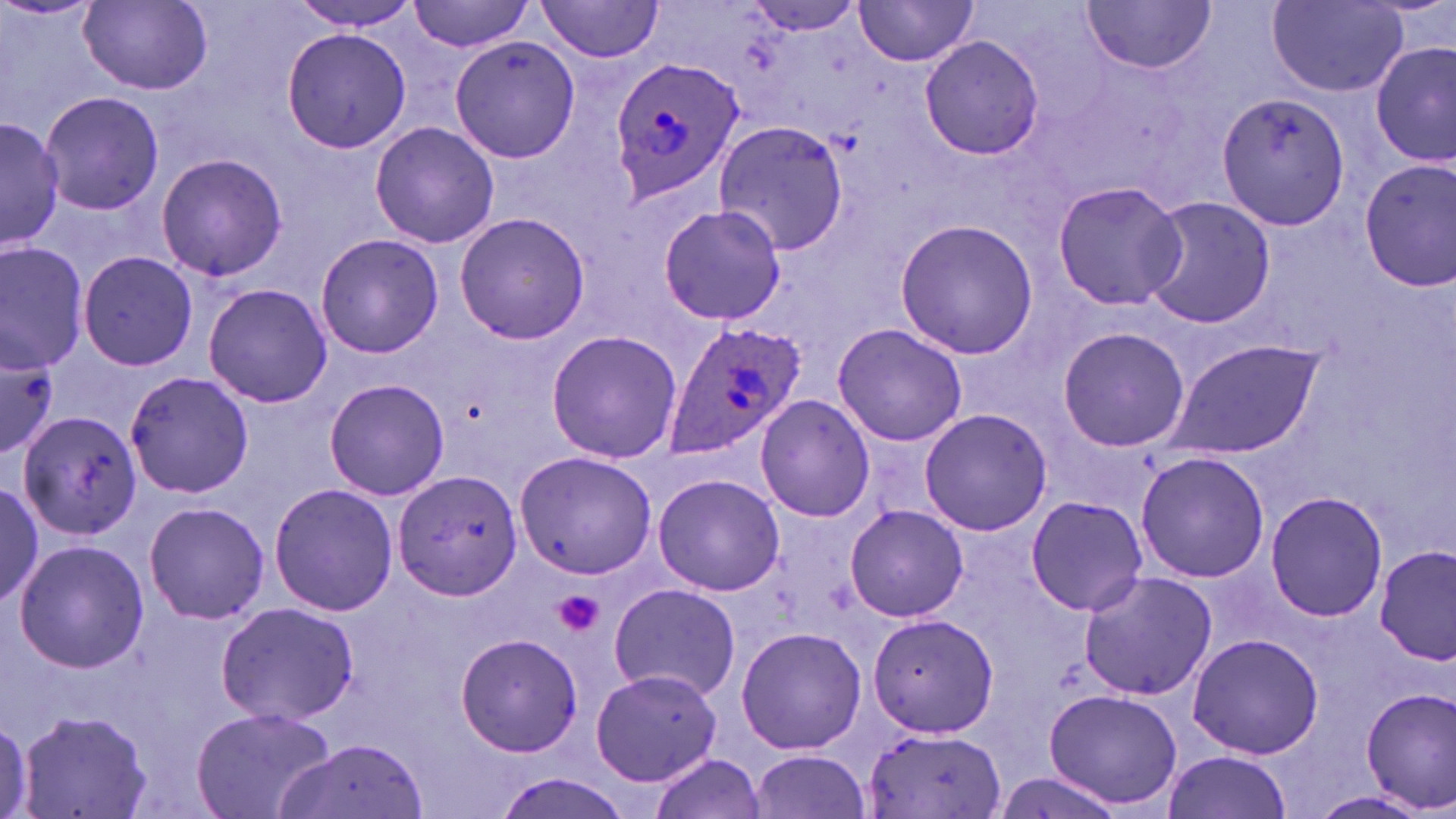
slide-level diagnosis = Plasmodium ovale
stain = May-Grünwald-Giemsa
image size = 1456×819 pixels
platelet locations = approximate bounding boxes as [x1, y1, x2, y2] in pixels: [553, 590, 604, 637]
field of view = single
Plasmodium ovale-infected red blood cell locations = approximate bounding boxes as [x1, y1, x2, y2] in pixels: [608, 58, 745, 202], [660, 319, 805, 457]
uninfected red blood cell locations = approximate bounding boxes as [x1, y1, x2, y2] in pixels: [292, 0, 418, 32], [406, 0, 537, 54], [535, 0, 666, 61], [1265, 0, 1411, 98], [852, 1, 982, 66], [1083, 2, 1215, 78], [78, 3, 213, 92], [279, 26, 411, 155], [918, 33, 1045, 162], [450, 35, 584, 164], [1373, 39, 1454, 169], [40, 92, 163, 214], [1217, 92, 1350, 229], [0, 114, 63, 251], [714, 120, 850, 254], [368, 121, 499, 248], [155, 152, 288, 283], [1357, 156, 1456, 290], [1052, 180, 1185, 312], [1141, 197, 1278, 329], [656, 204, 786, 325], [453, 210, 591, 344], [893, 219, 1040, 360], [314, 233, 444, 358], [0, 242, 88, 376], [78, 250, 198, 373], [203, 281, 334, 410], [832, 322, 967, 448], [1057, 325, 1189, 453], [545, 328, 684, 464], [1162, 339, 1323, 461], [0, 346, 60, 454], [125, 371, 256, 499], [322, 377, 450, 501], [755, 394, 876, 522], [919, 408, 1053, 536], [17, 409, 144, 540], [515, 449, 660, 580], [1133, 452, 1272, 583], [394, 471, 522, 602], [653, 472, 783, 597], [0, 478, 44, 608], [268, 483, 400, 616], [1264, 490, 1388, 623], [1024, 495, 1148, 615], [144, 501, 268, 625], [845, 504, 969, 624], [13, 539, 148, 672], [1376, 546, 1454, 665], [1078, 571, 1217, 700], [610, 582, 740, 700], [213, 601, 360, 726], [865, 611, 1001, 739], [736, 627, 868, 756], [455, 631, 584, 757], [1186, 633, 1324, 759], [590, 668, 725, 788], [1357, 686, 1455, 814], [1043, 688, 1183, 811], [190, 705, 334, 819], [18, 707, 151, 818], [1, 715, 34, 817], [861, 728, 1007, 819], [277, 736, 427, 819], [751, 749, 873, 818], [1162, 750, 1293, 819], [648, 751, 766, 819], [489, 770, 636, 819], [1312, 790, 1439, 817]
modality = optical microscopy
magnification = 1000x
preparation = thin blood smear